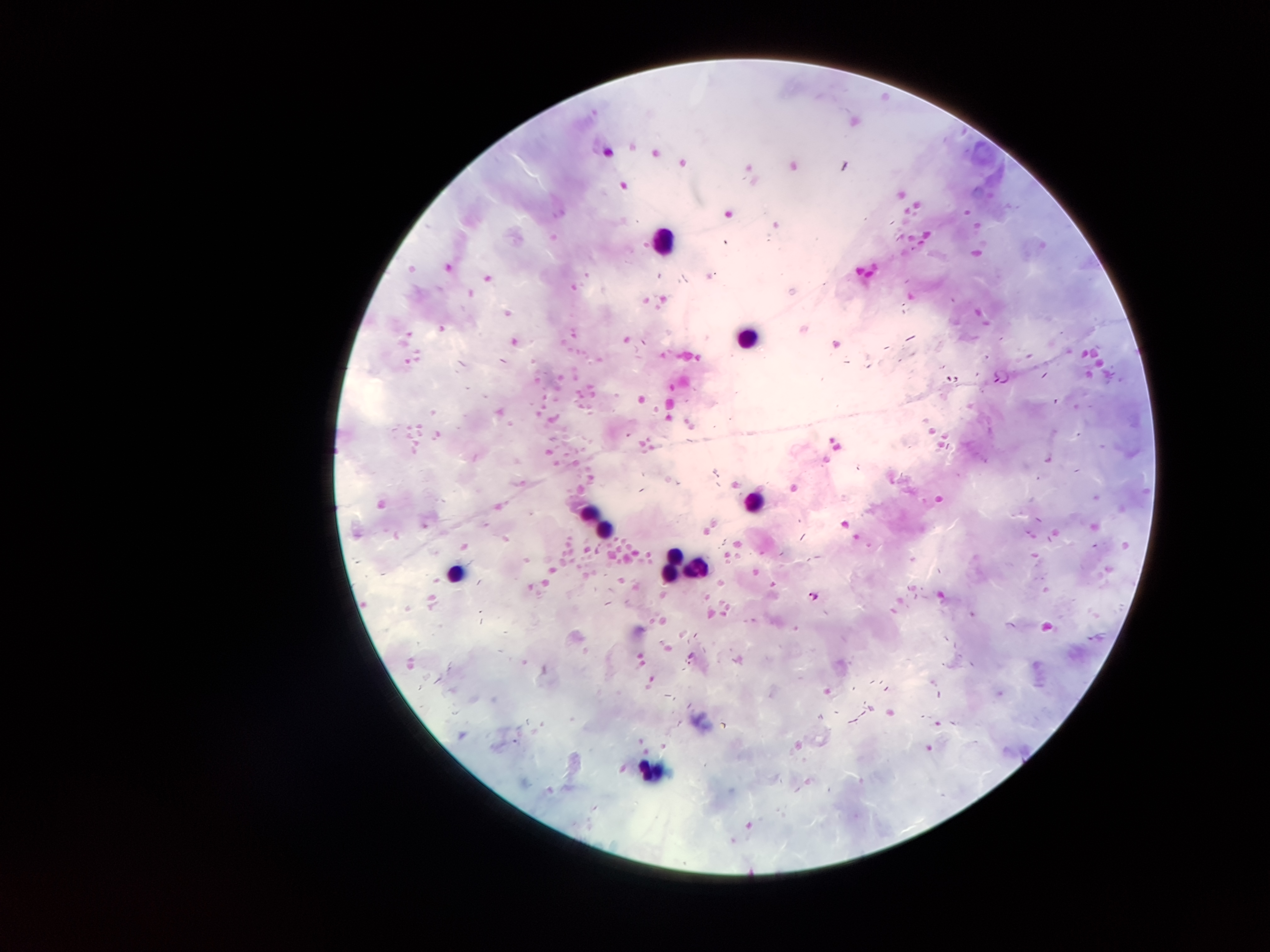

coordinate format = approximate centers as [x, y] in pixels
leukocyte locations = [658, 240], [750, 339], [753, 499], [587, 512], [603, 533], [674, 555], [698, 565], [669, 570], [453, 573], [650, 767]
malaria parasite locations = [814, 595]
image size = 1270×952 pixels
patient malaria status = infected with Plasmodium falciparum
stain = Giemsa
field of view = one from this slide
capture = smartphone through the microscope eyepiece
magnification = 100x
preparation = thick blood film